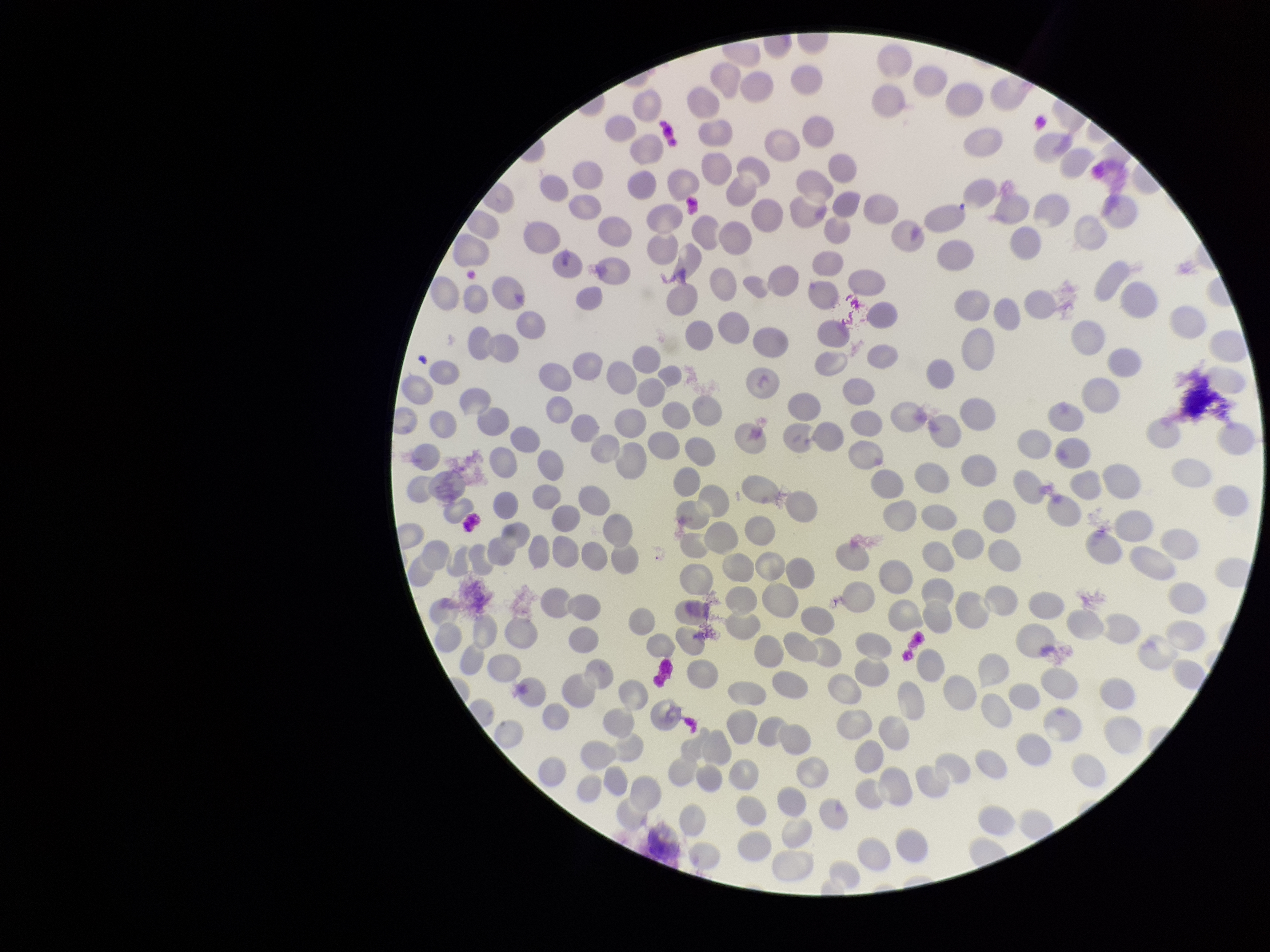

Summary:
  - Preparation: thin
  - Red blood cell count: 264
  - Field of view: single
  - Stain: Giemsa
  - Capture: smartphone photograph through the microscope eyepiece
  - Image size: 1270×952 pixels
  - Parasitized red blood cells: none detected
  - Parasitized red blood cell count: 0
  - Patient malaria status: negative